Identify the parasite.
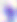
Toxoplasma gondii.

Captured at 400x magnification. Micrograph.